Classify this cell by malaria status.
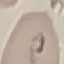

It is parasitized.

Summary:
  - Preparation: thin blood film
  - Capture: smartphone camera at the microscope eyepiece
  - Stain: Giemsa
  - Image type: cell patch, automatically extracted from a larger field of view and resized to 64 × 64 pixels